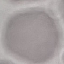
Summary:
  - Result: negative for malaria parasites
  - Preparation: thin blood film
  - Stain: Giemsa
  - Image type: cell patch, automatically extracted from a larger field of view and resized to 64 × 64 pixels
  - Capture: smartphone through the microscope eyepiece